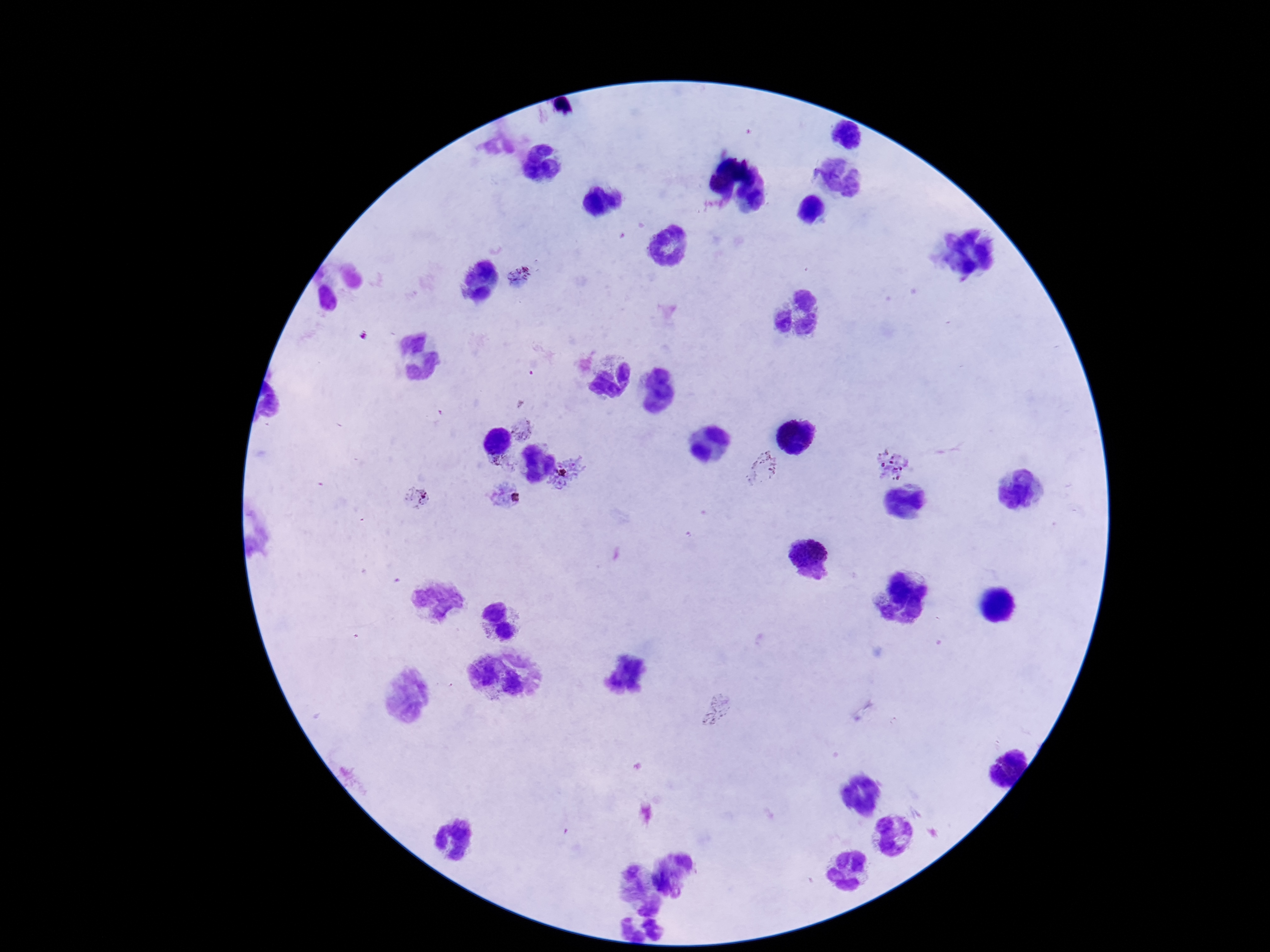
{
  "field_of_view": "one from this slide",
  "magnification": "100x",
  "image_size": "1270×952 pixels",
  "plasmodium_parasite_locations": "approximate centers as {x, y} in pixels: {519, 276}, {525, 429}, {501, 463}, {892, 463}, {762, 468}, {566, 478}, {504, 496}, {416, 497}, {716, 711}",
  "capture": "smartphone camera through the microscope eyepiece",
  "preparation": "thick blood smear",
  "patient_malaria_status": "positive",
  "stain": "Giemsa"
}